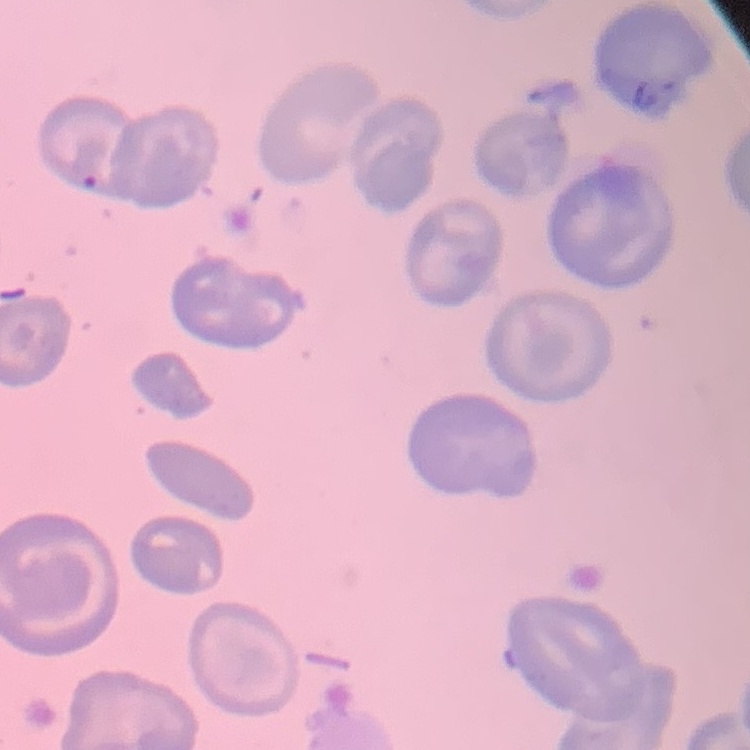

Summary:
  - Red blood cell morphology: no rouleaux formation
  - Stain: Field's or Giemsa
  - Preparation: thin blood film
  - Image type: square crop of a larger photomicrograph